Locate every Plasmodium parasite.
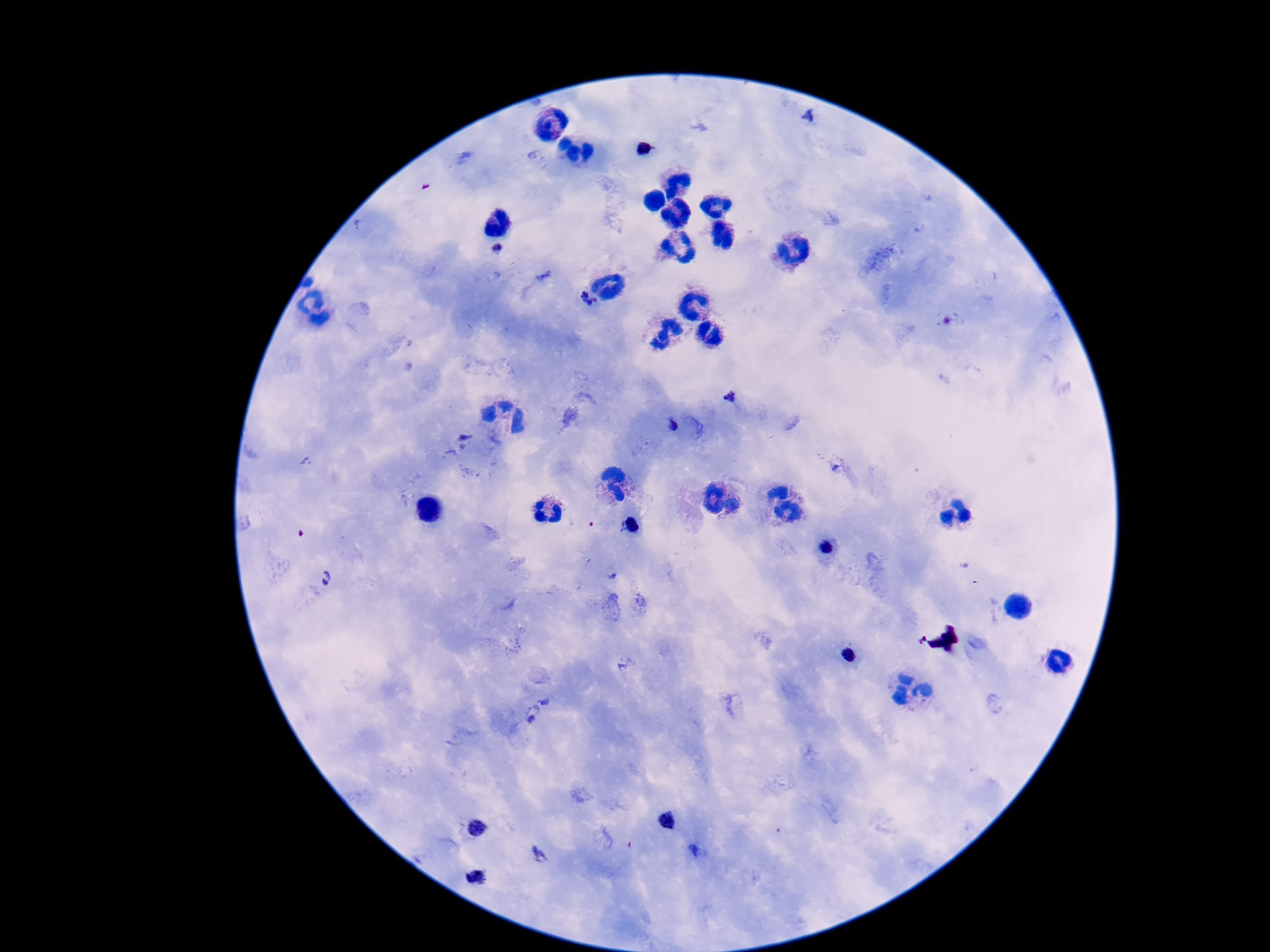

Approximate object centers, in pixels from the top-left corner.
Plasmodium parasites: (x=644, y=149), (x=497, y=249), (x=585, y=301), (x=729, y=395), (x=671, y=423), (x=630, y=527), (x=826, y=547), (x=326, y=579), (x=850, y=655), (x=668, y=820), (x=477, y=828), (x=693, y=850), (x=542, y=854), (x=477, y=877).

100x magnification. Single field of view. Image is 1270×952 pixels. Patient malaria status: positive. Thick blood smear. Photographed through the microscope eyepiece with a smartphone camera. Giemsa stain.